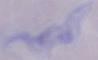
Summary:
  - Modality: micrograph
  - Magnification: 1000x
  - Identification: trypanosome